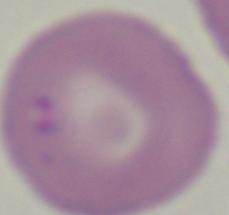
A Babesia parasite is shown. Photomicrograph. Captured at 1000x magnification.